Locate every blood parasite and identify its species.
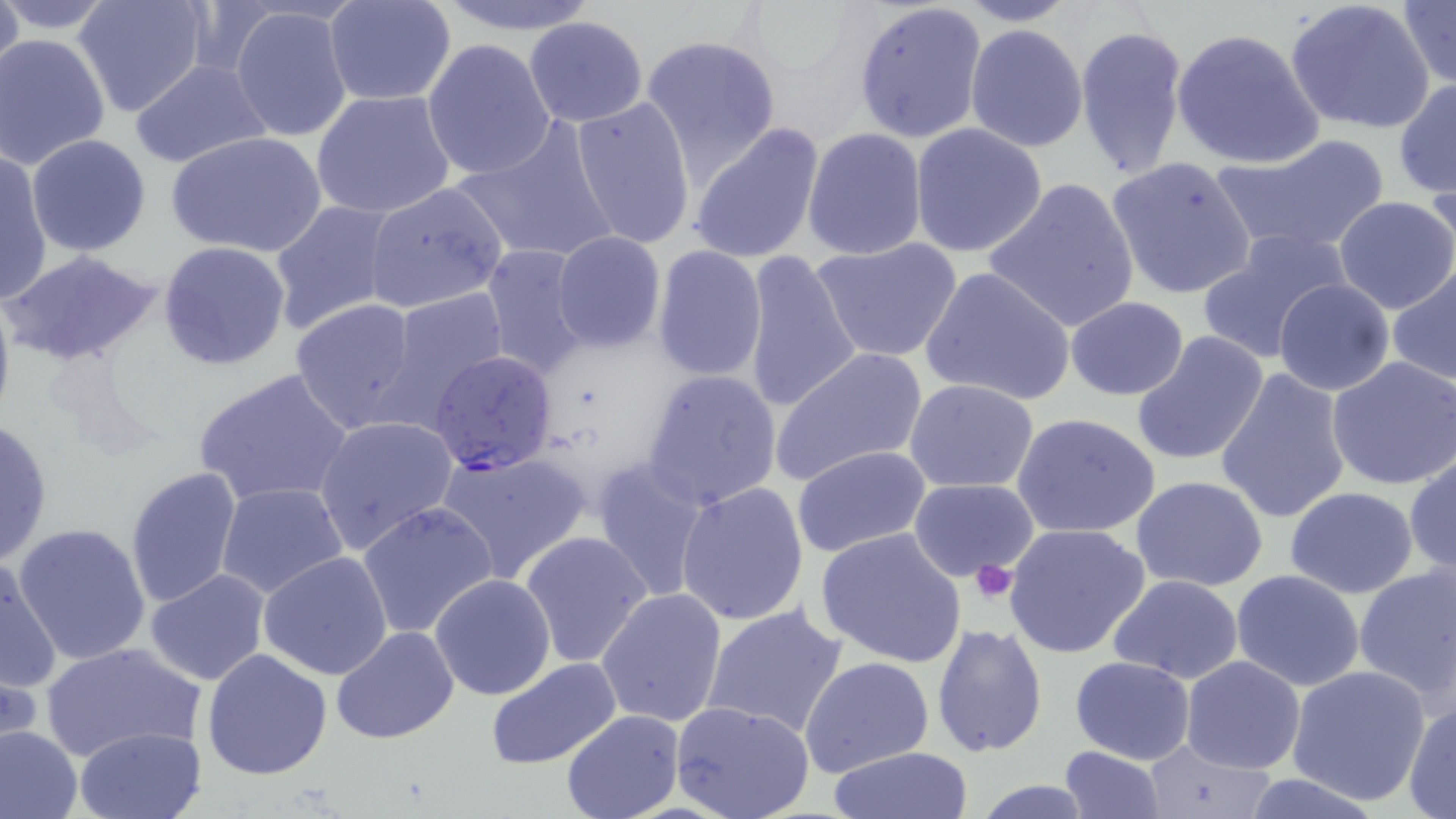

Approximate bounding boxes as [x1, y1, x2, y2] in pixels.
Plasmodium falciparum-infected red blood cells: [427, 352, 560, 477].
No Plasmodium ovale, Plasmodium malariae, Plasmodium vivax, Babesia divergens, or Trypanosoma brucei observed.

Summary:
  - Uninfected red blood cell locations: [1, 0, 24, 98], [73, 0, 212, 119], [429, 0, 601, 36], [852, 0, 987, 143], [956, 0, 1083, 26], [1285, 0, 1435, 134], [1398, 0, 1456, 89], [0, 1, 121, 36], [323, 1, 456, 108], [228, 5, 355, 144], [523, 15, 649, 127], [1074, 22, 1189, 182], [966, 23, 1088, 152], [1171, 27, 1325, 169], [1, 34, 109, 170], [641, 35, 781, 177], [421, 38, 557, 181], [129, 58, 272, 168], [1394, 77, 1455, 200], [311, 90, 456, 220], [570, 94, 696, 249], [450, 121, 618, 264], [908, 122, 1048, 259], [687, 124, 826, 265], [803, 127, 926, 260], [167, 130, 328, 261], [26, 133, 154, 257], [1211, 136, 1390, 255], [0, 150, 51, 307], [1106, 155, 1258, 301], [983, 178, 1142, 335], [362, 180, 508, 314], [1332, 196, 1456, 315], [266, 201, 396, 334], [1198, 228, 1355, 363], [551, 231, 666, 352], [809, 237, 964, 364], [156, 241, 291, 371], [481, 246, 591, 378], [651, 246, 767, 382], [3, 248, 164, 368], [739, 250, 864, 416], [919, 265, 1076, 407], [1388, 266, 1456, 387], [1273, 278, 1395, 396], [0, 279, 16, 431], [380, 287, 512, 421], [291, 296, 423, 433], [1065, 297, 1191, 402], [1130, 332, 1270, 467], [769, 348, 927, 486], [1326, 356, 1456, 489], [192, 367, 356, 510], [1213, 367, 1352, 525], [641, 368, 782, 511], [903, 378, 1041, 493], [1011, 412, 1162, 539], [313, 415, 460, 554], [0, 417, 55, 567], [792, 445, 930, 557], [435, 448, 591, 584], [1405, 453, 1456, 579], [591, 458, 710, 601], [124, 465, 243, 610], [1130, 474, 1269, 593], [907, 478, 1041, 582], [674, 481, 810, 626], [216, 482, 350, 602], [1284, 486, 1420, 598], [358, 501, 498, 639], [1002, 522, 1153, 660], [11, 523, 153, 668], [815, 527, 967, 669], [518, 530, 655, 669], [259, 552, 393, 681], [0, 555, 64, 699], [1352, 562, 1455, 702], [146, 568, 271, 687], [1231, 569, 1365, 690], [429, 573, 558, 701], [1105, 574, 1245, 684], [595, 587, 729, 728], [700, 602, 850, 739], [931, 623, 1048, 757], [331, 627, 460, 745], [39, 641, 205, 764], [202, 648, 333, 779], [800, 654, 935, 777], [1069, 656, 1196, 765], [1180, 656, 1307, 773], [485, 657, 623, 769], [1286, 664, 1432, 806], [671, 700, 816, 819], [1404, 700, 1456, 819], [559, 709, 686, 819], [0, 723, 84, 819], [74, 726, 205, 819], [1137, 739, 1277, 818], [828, 746, 974, 818], [1060, 746, 1166, 819], [968, 779, 1098, 818]
  - Platelet locations: [971, 561, 1019, 603]
  - Slide-level diagnosis: Plasmodium falciparum
  - Image size: 1456×819 pixels
  - Magnification: 1000x
  - Field of view: single
  - Preparation: thin blood film
  - Stain: May-Grünwald-Giemsa
  - Modality: light microscopy